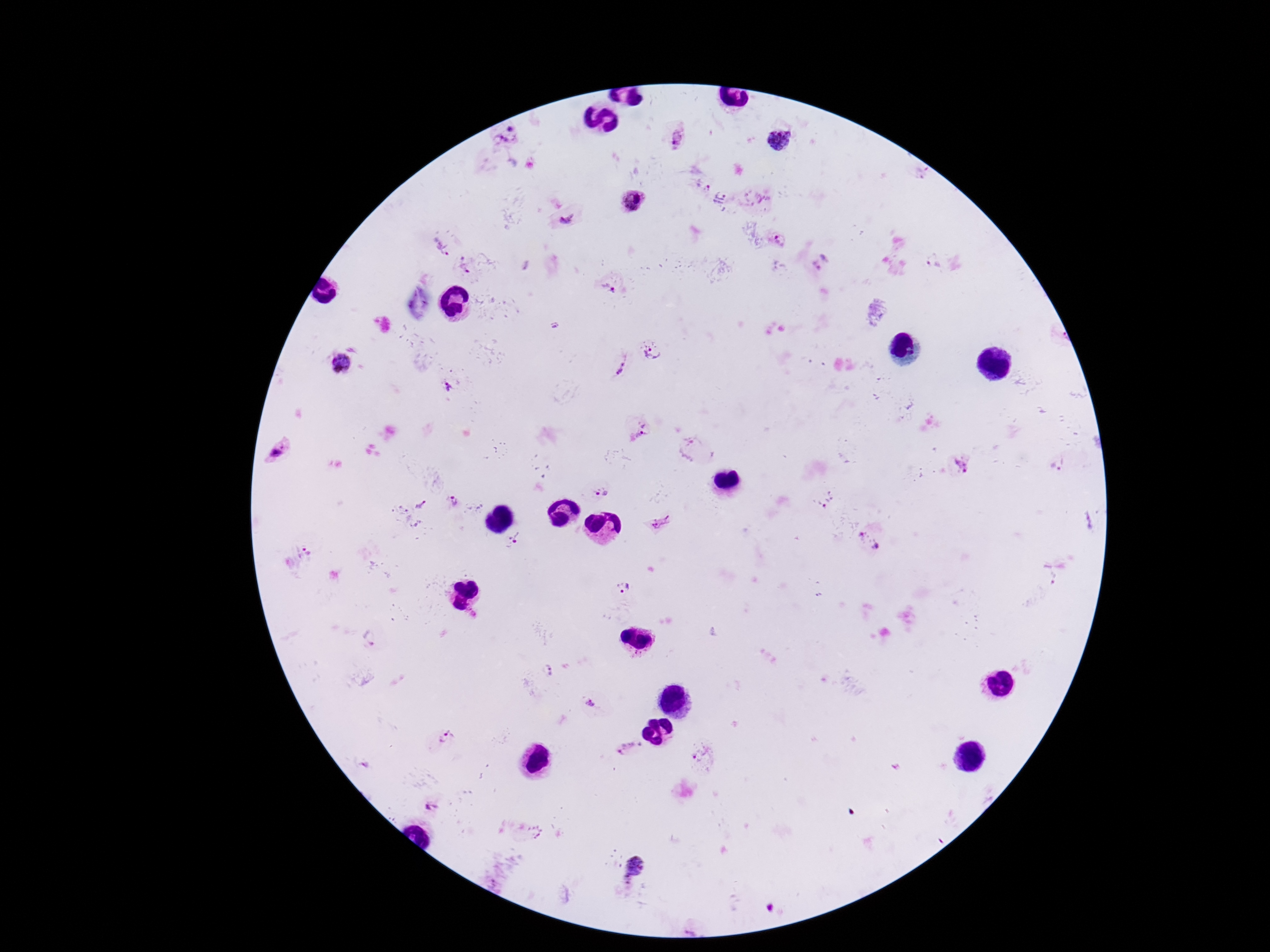

capture = smartphone camera through the microscope eyepiece
preparation = thick blood smear
Plasmodium parasite locations = approximate centers as [x, y] in pixels: [506, 135], [675, 139], [780, 141], [702, 185], [720, 199], [755, 199], [632, 200], [566, 218], [778, 236], [439, 245], [932, 261], [822, 262], [466, 266], [615, 293], [653, 350], [340, 363], [615, 364], [449, 386], [645, 427], [690, 447], [278, 450], [962, 466], [1058, 466], [598, 492], [825, 500], [451, 501], [420, 504], [659, 523], [516, 537], [870, 541], [309, 552], [624, 588], [370, 638], [547, 671], [591, 705], [443, 737], [627, 749], [700, 755], [433, 808], [633, 865]
image size = 1270×952 pixels
magnification = 100x
patient malaria status = positive
stain = Giemsa
field of view = single